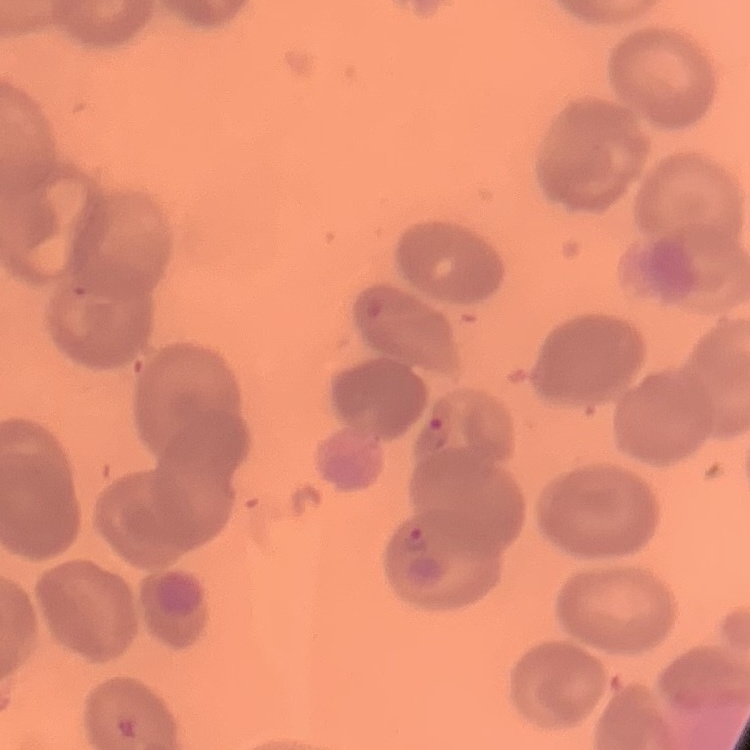

Summary:
  - Red blood cell morphology: no rouleaux formation
  - Stain: Field's or Giemsa
  - Image type: one tile cut from a larger photomicrograph
  - Preparation: thin blood smear